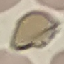

Summary:
  - Malaria status: uninfected
  - Stain: Giemsa
  - Preparation: thin blood smear
  - Image type: automatically extracted cell patch, resized to 64 × 64 pixels
  - Capture: smartphone through the microscope eyepiece